Outline each uninfected red blood cell.
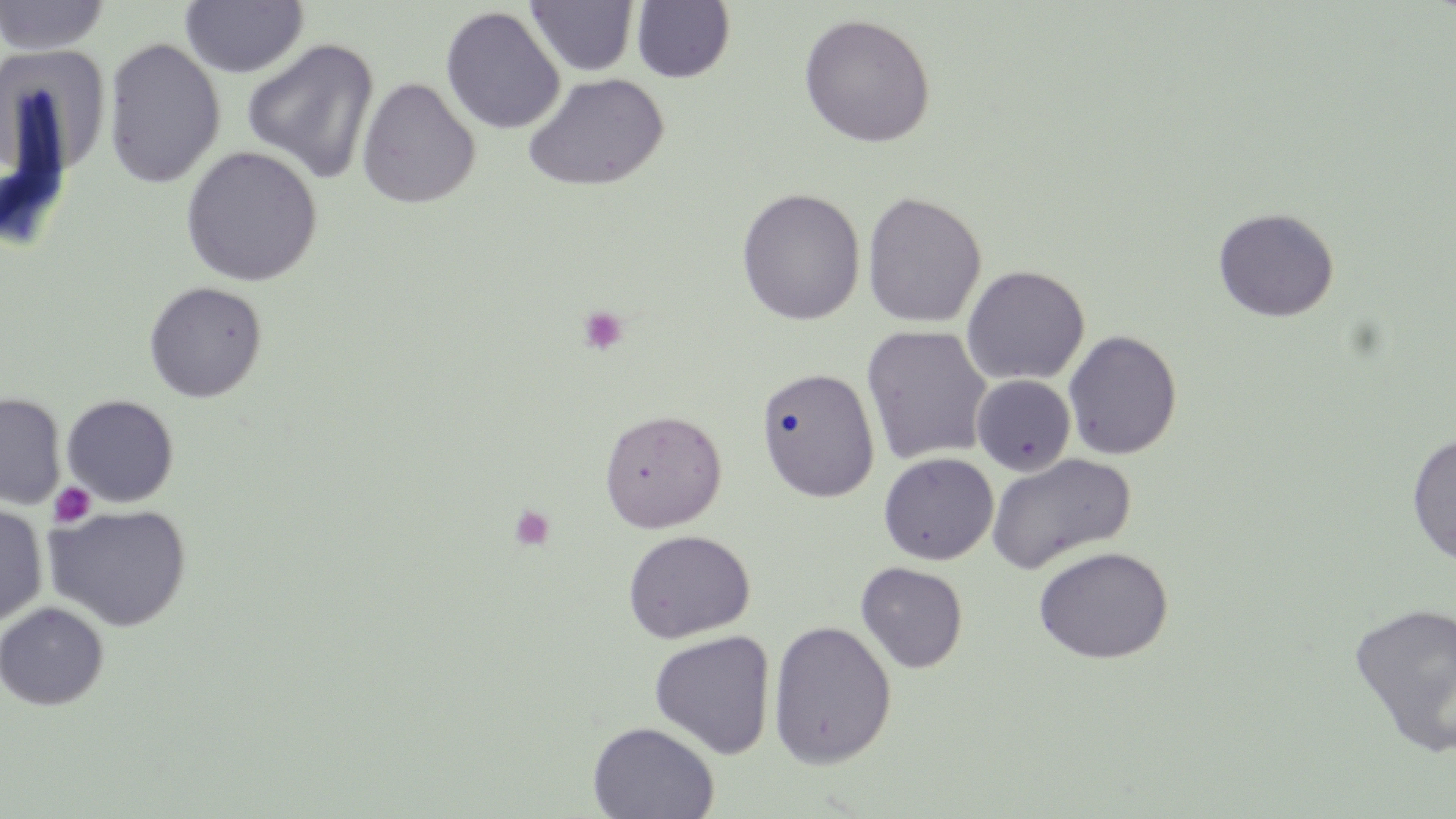
Approximate bounding boxes as (x1, y1, x2, y2) in pixels.
Uninfected red blood cells: (0, 0, 111, 56), (179, 1, 308, 79), (525, 1, 640, 77), (631, 1, 735, 84), (440, 5, 565, 135), (798, 13, 936, 148), (102, 38, 226, 190), (241, 38, 380, 184), (522, 72, 669, 192), (357, 77, 481, 208), (180, 145, 322, 287), (736, 187, 866, 325), (862, 191, 986, 328), (1213, 207, 1339, 322), (961, 264, 1090, 386), (143, 281, 268, 403), (861, 325, 993, 465), (1063, 330, 1183, 460), (755, 366, 880, 502), (971, 374, 1077, 476), (0, 392, 66, 509), (61, 394, 180, 507), (598, 408, 727, 533), (611, 409, 739, 647), (1406, 432, 1456, 565), (878, 452, 998, 565), (986, 453, 1136, 574), (0, 503, 48, 627), (45, 504, 192, 632), (623, 529, 755, 643), (1034, 546, 1174, 664), (856, 561, 969, 673), (1348, 601, 1456, 757), (0, 602, 109, 711), (767, 619, 897, 769), (650, 630, 775, 759), (586, 721, 720, 819).

slide-level diagnosis = no evidence of blood parasites
image size = 1456×819 pixels
magnification = 1000x
preparation = thin blood smear
stain = May-Grünwald-Giemsa
platelet locations = approximate bounding boxes as (x1, y1, x2, y2) in pixels: (577, 305, 629, 356), (49, 482, 96, 528), (509, 505, 555, 551)
modality = light microscopy
field of view = one of a larger specimen